Report the malaria status of this cell.
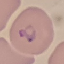
Parasitized.

capture: smartphone camera at the microscope eyepiece
preparation: thin smear
stain: Giemsa
image_type: automatically extracted cell patch, resized to 64 × 64 pixels